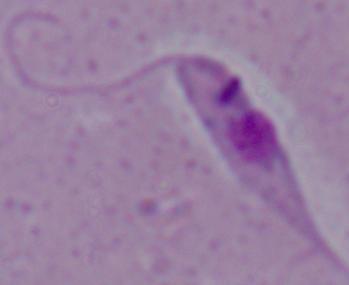
modality = micrograph
identification = Leishmania
magnification = 1000x